Classify this cell by malaria status.
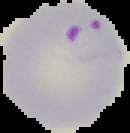
It is parasitized.

Summary:
  - Preparation: thin blood smear
  - Image size: 130×133 pixels
  - Image type: cell region segmented out of the field of view; surrounding area masked to black